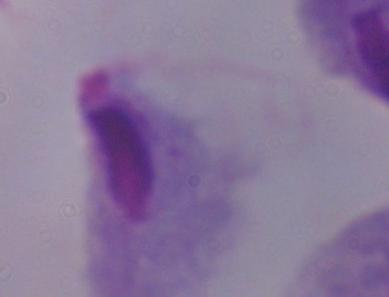
Summary:
  - Modality: micrograph
  - Identification: trichomonad
  - Magnification: 1000x